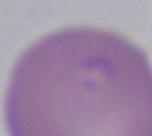

Summary:
  - Modality: photomicrograph
  - Identification: Babesia
  - Magnification: 1000x